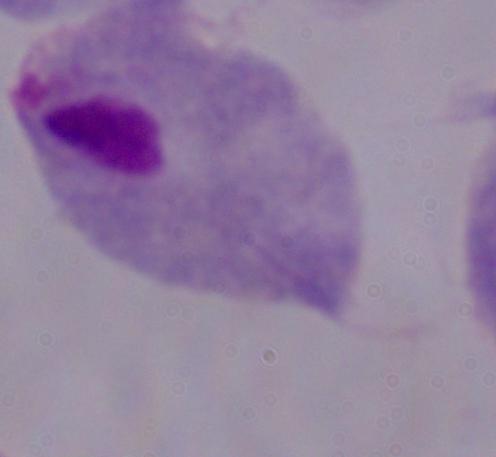

Summary:
  - Identification: trichomonad
  - Modality: photomicrograph
  - Magnification: 1000x